Assess the morphology of the red blood cells.
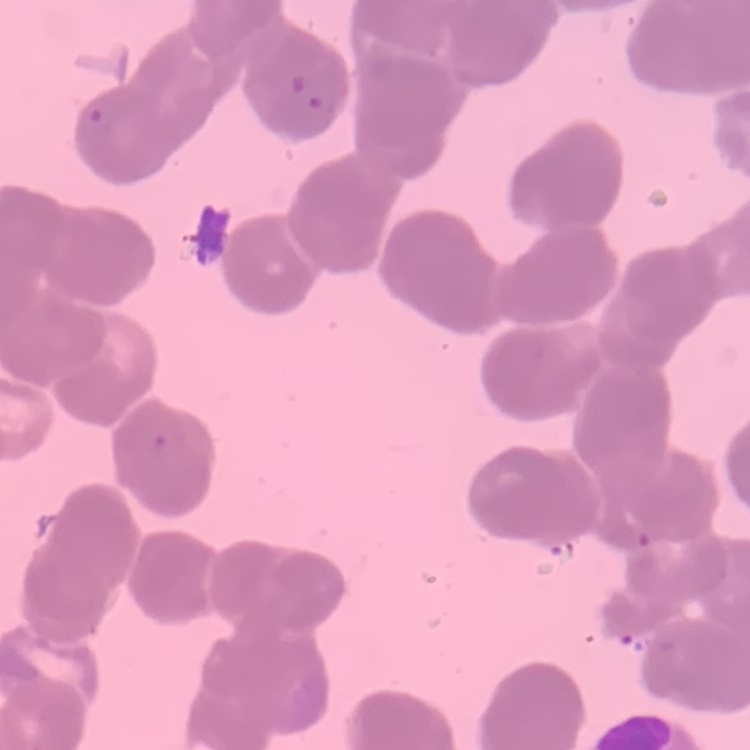

They show rouleaux formation.

Square crop of a larger photomicrograph. Stained with either Field's or Giemsa. Thin peripheral smear.